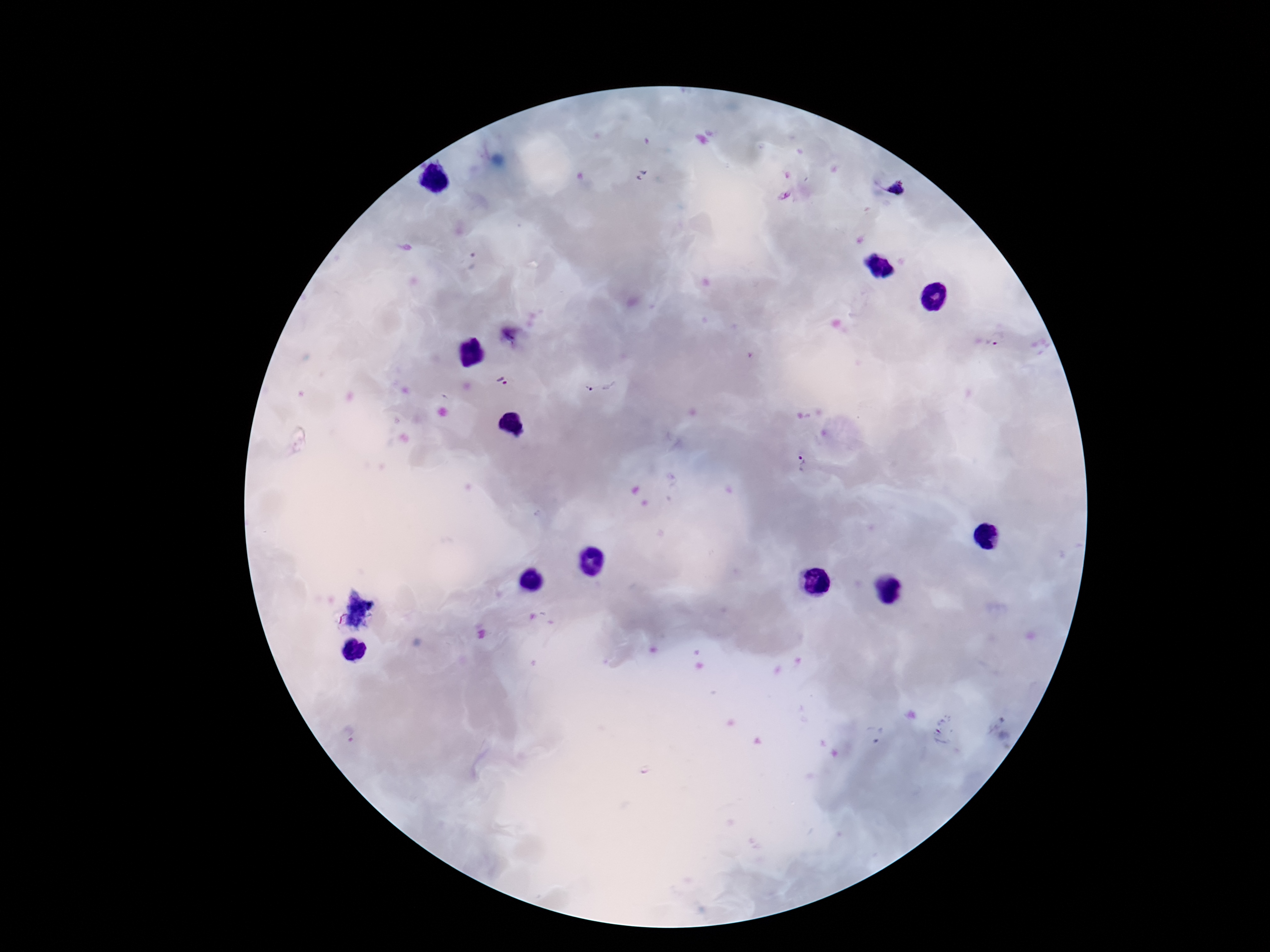
{
  "stain": "Giemsa",
  "field_of_view": "one from this slide",
  "magnification": "100x",
  "preparation": "thick blood film",
  "capture": "smartphone camera through the microscope eyepiece",
  "patient_malaria_status": "infected",
  "plasmodium_parasite_locations": "approximate centers as (x, y) in pixels: (898, 190), (784, 196), (473, 262), (997, 340), (504, 383), (598, 384), (802, 462), (942, 730), (875, 734), (348, 735)",
  "image_size": "1270×952 pixels"
}